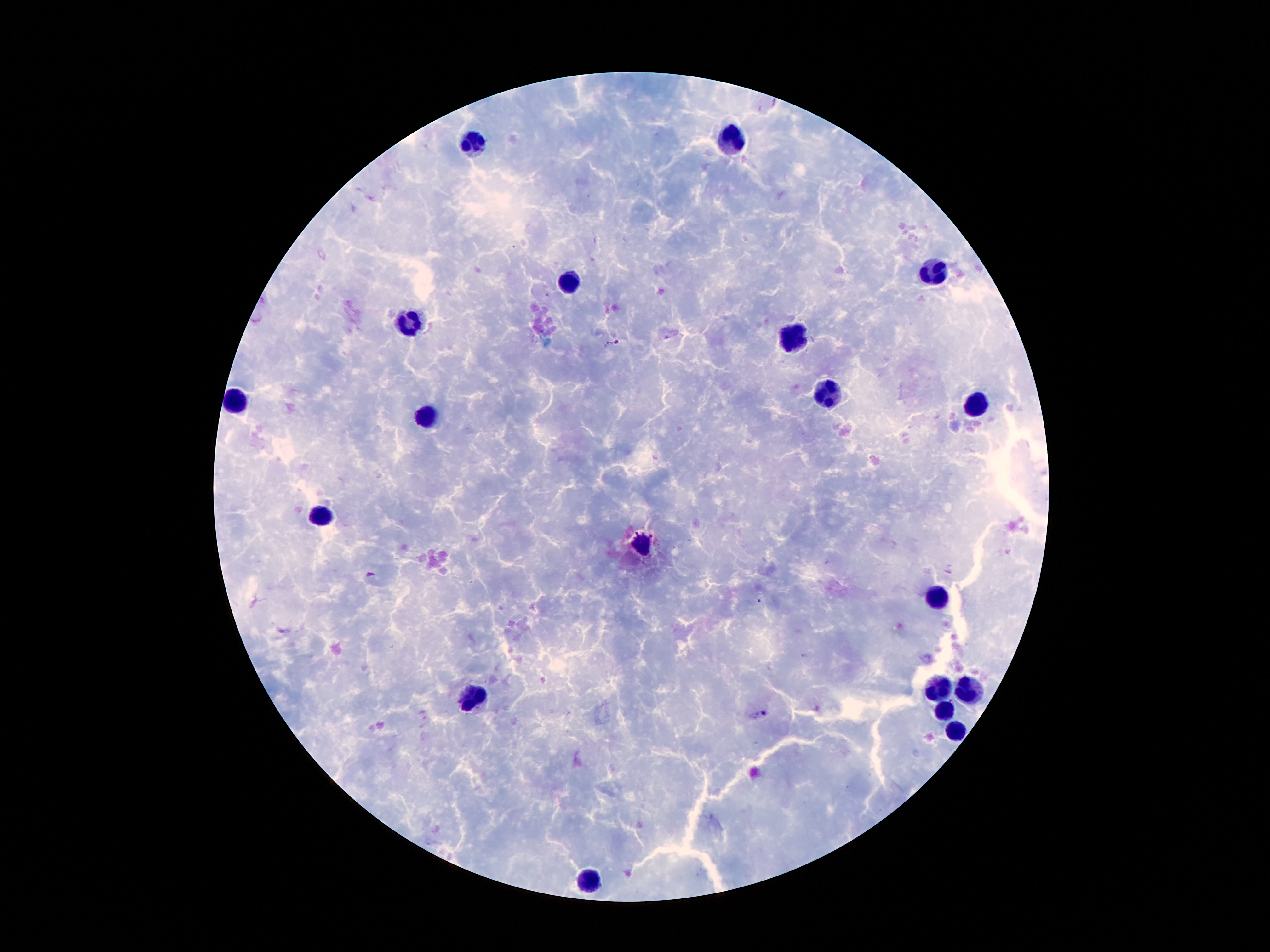

field_of_view: one from this slide
preparation: thick blood film
capture: smartphone through the microscope eyepiece
image_size: 1270×952 pixels
leukocyte_locations: 'approximate centers as (x, y) in pixels: (474, 139), (728, 139), (931, 273), (572, 284), (413, 321), (797, 338), (828, 395), (237, 401), (977, 401), (428, 412), (320, 517), (640, 544), (938, 599), (938, 683), (969, 687), (478, 691), (944, 712), (952, 729), (591, 884)'
stain: Giemsa
malaria_parasite_locations: 'approximate centers as (x, y) in pixels: (612, 343), (765, 713)'
magnification: 100x
patient_malaria_status: infected with Plasmodium falciparum